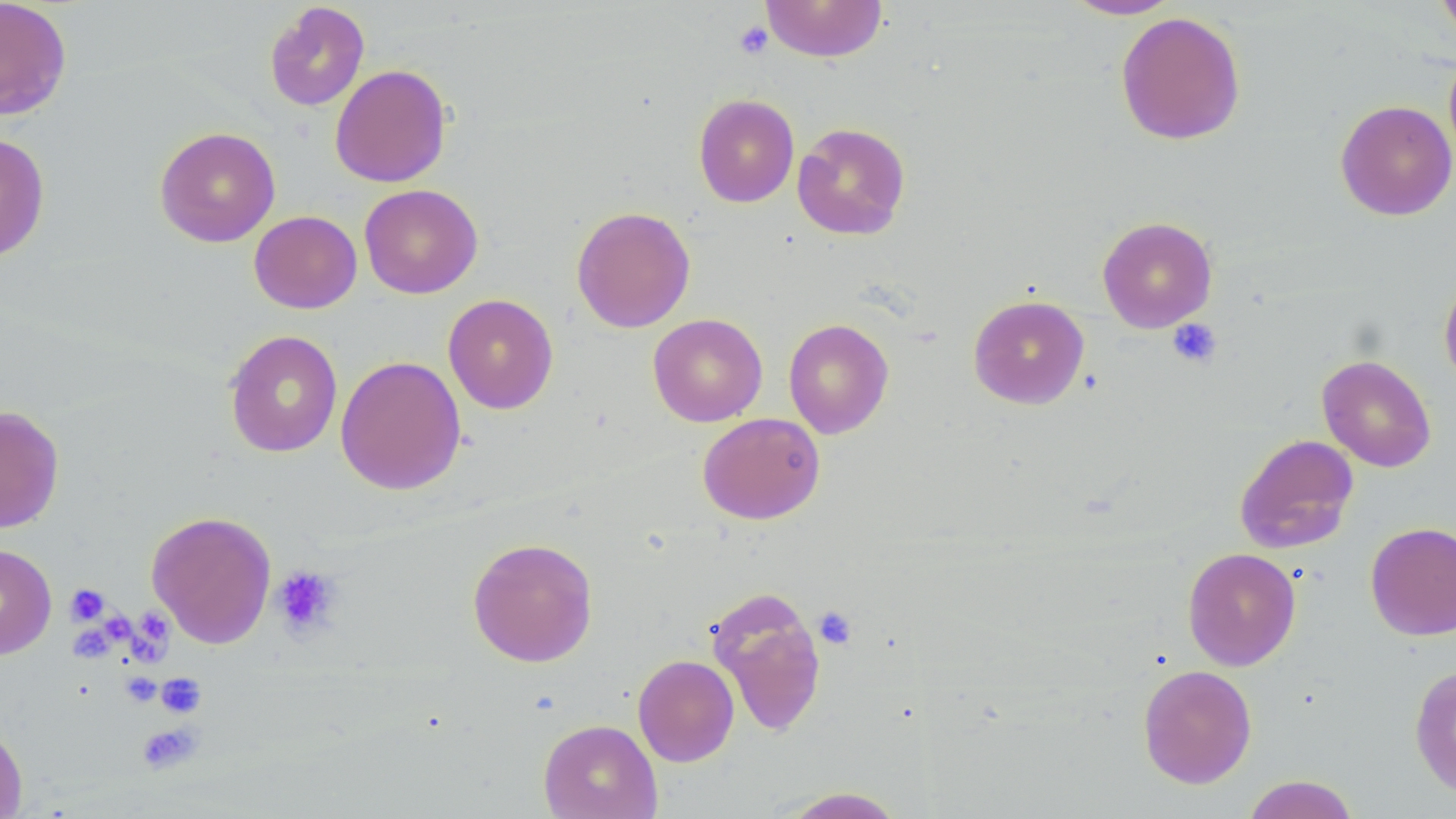

Summary:
  - Coordinate format: approximate bounding boxes as named x1/y1/x2/y2 corners in pixels
  - Platelet locations: (x1=734, y1=21, x2=774, y2=59), (x1=1168, y1=319, x2=1222, y2=368), (x1=271, y1=565, x2=342, y2=639), (x1=66, y1=584, x2=109, y2=625), (x1=812, y1=607, x2=858, y2=650), (x1=106, y1=612, x2=137, y2=643), (x1=142, y1=612, x2=173, y2=644), (x1=71, y1=625, x2=115, y2=666), (x1=131, y1=632, x2=172, y2=671), (x1=122, y1=673, x2=163, y2=708), (x1=156, y1=673, x2=207, y2=718), (x1=136, y1=722, x2=202, y2=774)
  - Uninfected red blood cell locations: (x1=0, y1=0, x2=72, y2=120), (x1=761, y1=0, x2=888, y2=62), (x1=1060, y1=0, x2=1182, y2=20), (x1=1434, y1=0, x2=1456, y2=42), (x1=264, y1=2, x2=370, y2=111), (x1=1115, y1=11, x2=1246, y2=145), (x1=329, y1=64, x2=452, y2=188), (x1=693, y1=93, x2=799, y2=207), (x1=1335, y1=99, x2=1456, y2=221), (x1=792, y1=121, x2=911, y2=241), (x1=154, y1=126, x2=281, y2=247), (x1=0, y1=131, x2=51, y2=263), (x1=359, y1=183, x2=483, y2=299), (x1=570, y1=206, x2=695, y2=333), (x1=249, y1=210, x2=362, y2=313), (x1=1097, y1=216, x2=1218, y2=333), (x1=1439, y1=271, x2=1456, y2=390), (x1=443, y1=294, x2=559, y2=414), (x1=968, y1=294, x2=1090, y2=409), (x1=647, y1=313, x2=767, y2=427), (x1=783, y1=318, x2=894, y2=439), (x1=224, y1=329, x2=343, y2=458), (x1=1317, y1=354, x2=1437, y2=472), (x1=335, y1=355, x2=467, y2=495), (x1=0, y1=405, x2=65, y2=534), (x1=697, y1=412, x2=825, y2=525), (x1=1234, y1=433, x2=1359, y2=554), (x1=146, y1=510, x2=277, y2=648), (x1=1365, y1=521, x2=1456, y2=641), (x1=467, y1=536, x2=599, y2=668), (x1=0, y1=543, x2=57, y2=659), (x1=1183, y1=548, x2=1301, y2=670), (x1=705, y1=586, x2=828, y2=738), (x1=633, y1=654, x2=739, y2=767), (x1=1409, y1=663, x2=1456, y2=799), (x1=1138, y1=664, x2=1257, y2=789), (x1=538, y1=718, x2=662, y2=819), (x1=0, y1=720, x2=28, y2=818), (x1=1240, y1=774, x2=1361, y2=819), (x1=774, y1=786, x2=909, y2=818)
  - Slide-level diagnosis: no evidence of blood parasites
  - Stain: May-Grünwald-Giemsa
  - Magnification: 1000x
  - Image size: 1456×819 pixels
  - Modality: optical microscopy
  - Field of view: one of a larger specimen
  - Preparation: thin blood smear